Comment on the morphology of the red blood cells.
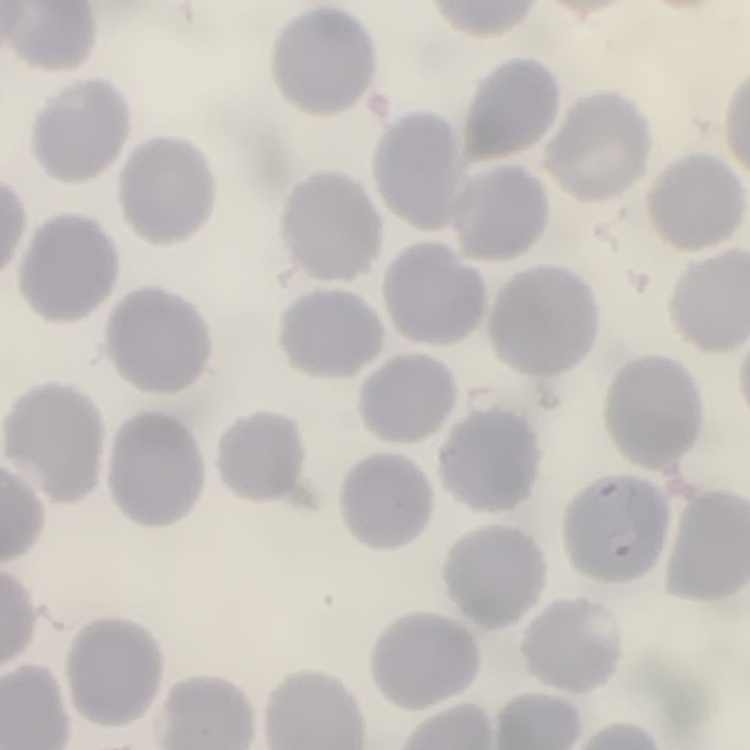
No rouleaux formation.

Summary:
  - Stain: Field's or Giemsa
  - Preparation: thin blood smear
  - Image type: square crop of a larger photomicrograph